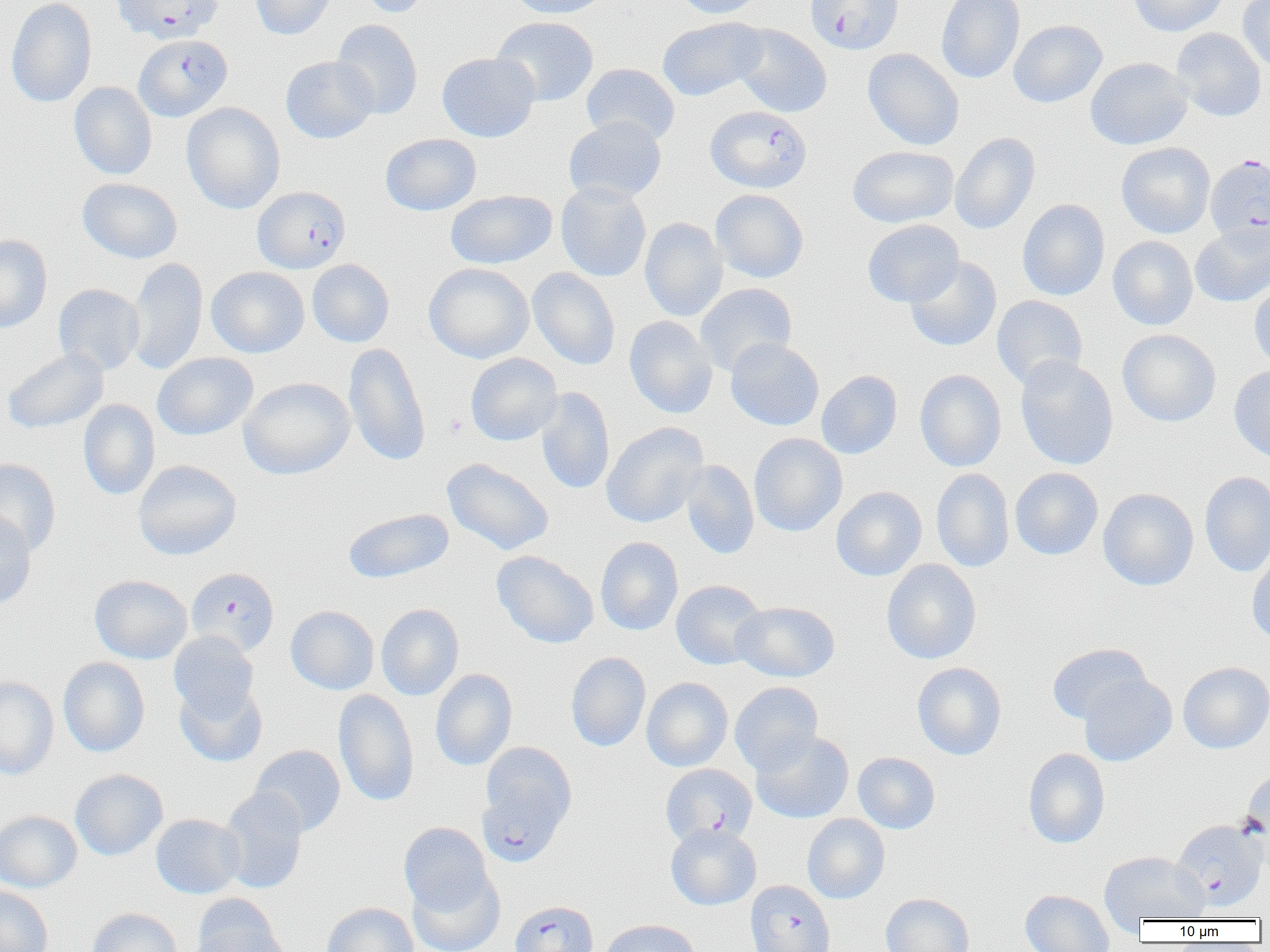

slide-level diagnosis = Plasmodium falciparum
field of view = one of a larger specimen
preparation = thin blood smear
uninfected red blood cell locations = approximate bounding boxes as [x1, y1, x2, y2] in pixels: [6, 0, 96, 108], [250, 0, 339, 40], [355, 0, 435, 18], [507, 0, 610, 18], [673, 0, 768, 19], [936, 0, 1025, 84], [1128, 0, 1229, 37], [1238, 0, 1270, 73], [491, 16, 599, 106], [657, 17, 767, 101], [332, 19, 423, 119], [1008, 20, 1107, 108], [731, 24, 832, 118], [1171, 28, 1267, 122], [862, 48, 964, 150], [437, 52, 539, 142], [281, 56, 379, 144], [1085, 57, 1193, 150], [581, 63, 680, 146], [69, 81, 157, 180], [181, 102, 285, 214], [564, 116, 666, 204], [950, 132, 1040, 234], [380, 133, 482, 216], [1116, 142, 1215, 238], [847, 145, 959, 228], [77, 178, 182, 264], [555, 183, 651, 282], [710, 189, 809, 283], [445, 190, 558, 269], [1017, 199, 1110, 301], [639, 217, 727, 321], [862, 219, 964, 307], [1190, 223, 1270, 307], [0, 234, 52, 333], [1108, 236, 1198, 330], [904, 256, 1002, 352], [126, 257, 208, 375], [307, 259, 394, 347], [424, 262, 534, 363], [206, 266, 309, 358], [527, 268, 620, 370], [1248, 277, 1270, 371], [694, 282, 797, 376], [53, 284, 144, 374], [992, 295, 1088, 390], [624, 316, 718, 419], [1117, 329, 1221, 427], [725, 338, 824, 431], [343, 343, 431, 467], [2, 347, 109, 434], [152, 352, 258, 440], [465, 353, 562, 446], [1015, 356, 1119, 470], [1229, 366, 1270, 464], [915, 369, 1007, 472], [816, 370, 902, 459], [238, 376, 355, 480], [535, 387, 615, 494], [78, 399, 160, 500], [600, 422, 709, 528], [749, 433, 848, 537], [0, 457, 61, 557], [442, 458, 554, 555], [133, 459, 242, 560], [679, 460, 759, 559], [1010, 467, 1103, 560], [931, 468, 1014, 572], [1199, 471, 1270, 577], [831, 486, 927, 581], [1097, 488, 1199, 591], [342, 508, 453, 584], [0, 510, 36, 610], [595, 537, 683, 635], [1246, 548, 1270, 646], [491, 550, 599, 649], [881, 559, 981, 664], [89, 574, 192, 664], [671, 580, 767, 670], [732, 601, 840, 682], [376, 604, 464, 700], [285, 605, 379, 695], [169, 631, 260, 722], [1047, 643, 1151, 725], [565, 652, 651, 752], [58, 657, 150, 757], [912, 662, 1007, 760], [1178, 662, 1270, 754], [430, 668, 517, 770], [1079, 673, 1177, 766], [0, 676, 59, 779], [642, 677, 733, 771], [175, 680, 267, 766], [730, 681, 823, 775], [333, 689, 419, 808], [751, 731, 853, 823], [249, 744, 346, 836], [1023, 748, 1110, 848], [853, 752, 940, 834], [70, 769, 168, 860], [1240, 769, 1270, 871], [217, 787, 309, 894], [0, 810, 82, 892], [151, 814, 246, 899], [802, 814, 889, 904], [399, 822, 493, 915], [666, 823, 761, 910], [1099, 851, 1210, 926], [407, 866, 505, 952], [0, 886, 53, 952], [1019, 889, 1114, 952], [880, 893, 974, 952], [191, 896, 289, 952], [321, 902, 419, 952], [87, 908, 182, 952], [598, 919, 700, 952]
magnification = 1000x
modality = light microscopy
image size = 1270×952 pixels
Plasmodium falciparum-infected red blood cell locations = approximate bounding boxes as [x1, y1, x2, y2] in pixels: [112, 0, 222, 44], [806, 0, 904, 55], [133, 34, 232, 122], [706, 105, 812, 193], [1205, 153, 1270, 249], [253, 186, 351, 273], [186, 567, 280, 656], [480, 741, 577, 861], [661, 764, 757, 846], [1175, 821, 1270, 912], [745, 880, 835, 952], [509, 900, 598, 952]
platelet locations = approximate bounding boxes as [x1, y1, x2, y2] in pixels: [444, 414, 466, 437]